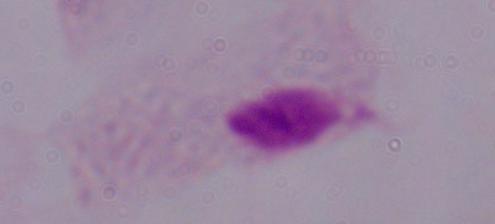
Summary:
  - Modality: photomicrograph
  - Identification: trichomonad
  - Magnification: 1000x